Assess this cell for malaria.
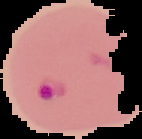
Parasitized.

image size = 142×139 pixels
preparation = thin blood film
image type = segmented cell region on a black background